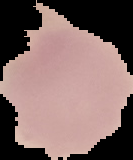
From a thin blood smear. Image is 133×160 pixels. Segmented cell region on a black background. Result: no Plasmodium parasites detected.